Name the blood parasite species.
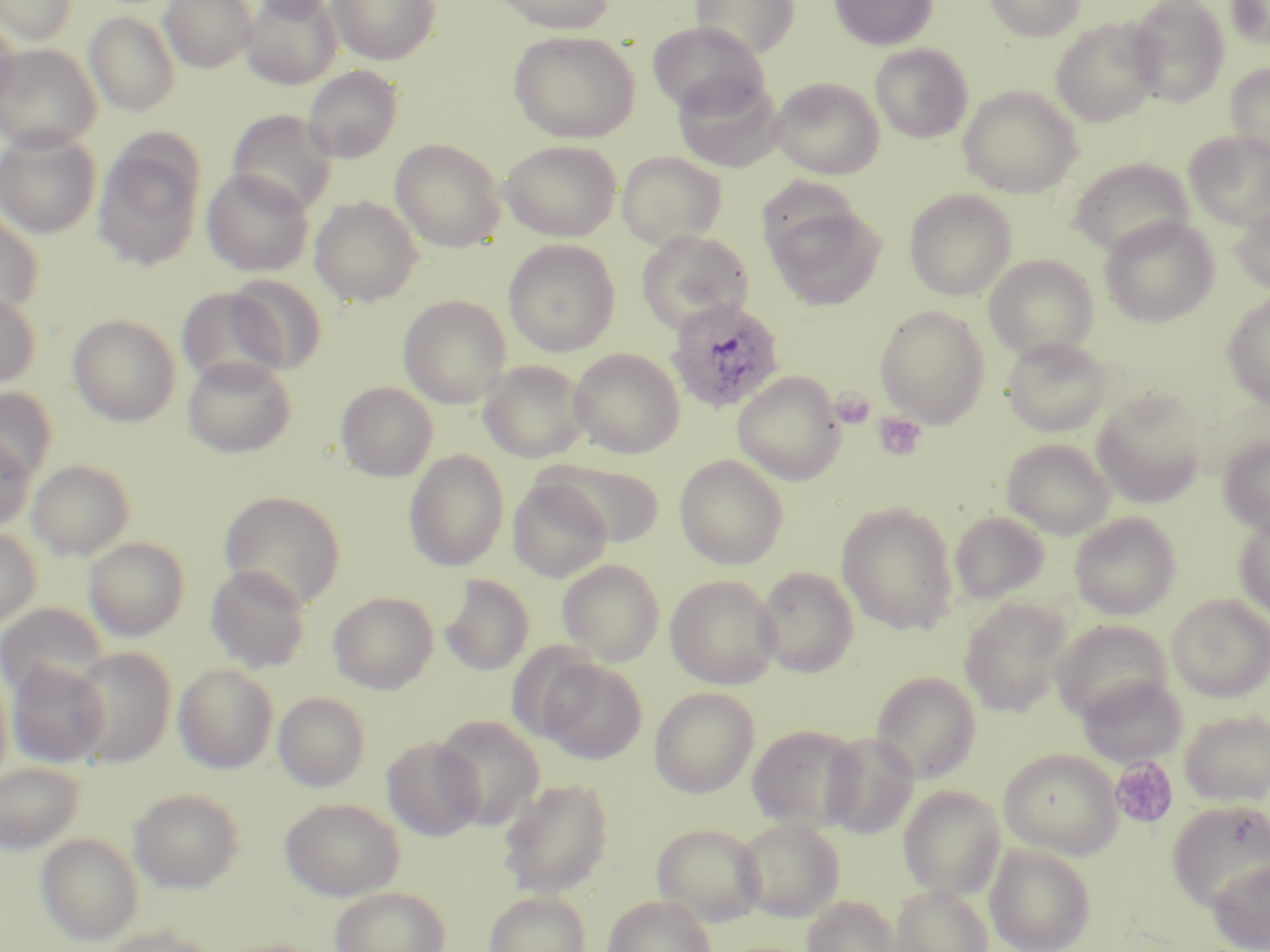

Plasmodium ovale.

Approximate bounding boxes as named x1/y1/x2/y2 corners in pixels. Platelet locations: (x1=831, y1=388, x2=876, y2=429), (x1=873, y1=413, x2=927, y2=461), (x1=1110, y1=756, x2=1179, y2=830). Uninfected red blood cell locations: (x1=1, y1=0, x2=78, y2=45), (x1=160, y1=0, x2=257, y2=73), (x1=241, y1=0, x2=342, y2=89), (x1=247, y1=0, x2=341, y2=19), (x1=328, y1=0, x2=441, y2=65), (x1=490, y1=0, x2=617, y2=34), (x1=690, y1=0, x2=800, y2=59), (x1=830, y1=0, x2=937, y2=51), (x1=984, y1=0, x2=1085, y2=41), (x1=1127, y1=0, x2=1229, y2=106), (x1=1226, y1=0, x2=1270, y2=50), (x1=84, y1=11, x2=181, y2=116), (x1=0, y1=16, x2=19, y2=115), (x1=1050, y1=17, x2=1164, y2=127), (x1=647, y1=21, x2=769, y2=118), (x1=508, y1=30, x2=641, y2=144), (x1=0, y1=43, x2=100, y2=151), (x1=871, y1=44, x2=972, y2=143), (x1=1225, y1=64, x2=1270, y2=162), (x1=302, y1=65, x2=403, y2=164), (x1=674, y1=74, x2=783, y2=173), (x1=770, y1=77, x2=885, y2=179), (x1=959, y1=86, x2=1082, y2=198), (x1=227, y1=109, x2=338, y2=217), (x1=0, y1=127, x2=102, y2=238), (x1=1184, y1=131, x2=1270, y2=229), (x1=391, y1=139, x2=506, y2=252), (x1=500, y1=139, x2=621, y2=241), (x1=93, y1=142, x2=205, y2=271), (x1=617, y1=151, x2=727, y2=249), (x1=1068, y1=157, x2=1194, y2=258), (x1=201, y1=168, x2=315, y2=277), (x1=904, y1=189, x2=1017, y2=301), (x1=310, y1=196, x2=424, y2=307), (x1=767, y1=203, x2=886, y2=311), (x1=1230, y1=204, x2=1270, y2=293), (x1=0, y1=210, x2=43, y2=318), (x1=1100, y1=216, x2=1219, y2=327), (x1=636, y1=230, x2=753, y2=334), (x1=504, y1=239, x2=621, y2=357), (x1=983, y1=254, x2=1099, y2=361), (x1=227, y1=274, x2=327, y2=373), (x1=175, y1=287, x2=290, y2=390), (x1=0, y1=289, x2=41, y2=389), (x1=1222, y1=292, x2=1270, y2=409), (x1=398, y1=295, x2=512, y2=408), (x1=874, y1=305, x2=990, y2=427), (x1=68, y1=314, x2=181, y2=427), (x1=1002, y1=336, x2=1111, y2=436), (x1=568, y1=348, x2=685, y2=458), (x1=182, y1=356, x2=296, y2=458), (x1=479, y1=360, x2=589, y2=463), (x1=732, y1=372, x2=846, y2=485), (x1=336, y1=381, x2=437, y2=481), (x1=0, y1=387, x2=57, y2=484), (x1=1091, y1=388, x2=1207, y2=507), (x1=0, y1=432, x2=35, y2=532), (x1=1219, y1=435, x2=1270, y2=537), (x1=1001, y1=438, x2=1115, y2=538), (x1=404, y1=449, x2=509, y2=572), (x1=674, y1=454, x2=789, y2=569), (x1=536, y1=458, x2=666, y2=546), (x1=28, y1=459, x2=135, y2=560), (x1=508, y1=478, x2=613, y2=582), (x1=219, y1=490, x2=346, y2=609), (x1=837, y1=502, x2=958, y2=634), (x1=950, y1=510, x2=1049, y2=605), (x1=1070, y1=513, x2=1180, y2=619), (x1=1234, y1=513, x2=1270, y2=621), (x1=0, y1=526, x2=41, y2=630), (x1=84, y1=537, x2=188, y2=642), (x1=557, y1=559, x2=665, y2=664), (x1=206, y1=564, x2=312, y2=672), (x1=558, y1=564, x2=780, y2=673), (x1=754, y1=566, x2=859, y2=677), (x1=439, y1=574, x2=534, y2=676), (x1=665, y1=574, x2=781, y2=689), (x1=328, y1=591, x2=438, y2=694), (x1=1168, y1=594, x2=1270, y2=701), (x1=958, y1=597, x2=1071, y2=717), (x1=0, y1=603, x2=107, y2=699), (x1=1051, y1=619, x2=1174, y2=723), (x1=69, y1=647, x2=175, y2=767), (x1=537, y1=656, x2=646, y2=763), (x1=6, y1=661, x2=110, y2=768), (x1=173, y1=663, x2=278, y2=773), (x1=0, y1=665, x2=13, y2=788), (x1=871, y1=672, x2=981, y2=783), (x1=1077, y1=673, x2=1188, y2=768), (x1=649, y1=687, x2=759, y2=798), (x1=273, y1=691, x2=370, y2=791), (x1=1180, y1=708, x2=1270, y2=805), (x1=434, y1=715, x2=545, y2=828), (x1=748, y1=724, x2=864, y2=831), (x1=820, y1=732, x2=919, y2=838), (x1=382, y1=736, x2=485, y2=841), (x1=998, y1=749, x2=1122, y2=857), (x1=0, y1=762, x2=85, y2=855), (x1=499, y1=778, x2=614, y2=897), (x1=898, y1=785, x2=1005, y2=898), (x1=129, y1=788, x2=245, y2=893), (x1=280, y1=797, x2=404, y2=900), (x1=1167, y1=800, x2=1270, y2=911), (x1=734, y1=818, x2=845, y2=921), (x1=653, y1=823, x2=766, y2=925), (x1=36, y1=833, x2=144, y2=946), (x1=985, y1=843, x2=1096, y2=952), (x1=1208, y1=856, x2=1270, y2=952), (x1=889, y1=884, x2=993, y2=952), (x1=330, y1=886, x2=451, y2=952), (x1=484, y1=891, x2=591, y2=952), (x1=603, y1=895, x2=717, y2=952), (x1=803, y1=896, x2=899, y2=952), (x1=100, y1=925, x2=220, y2=952). Plasmodium ovale-infected red blood cell locations: (x1=666, y1=298, x2=785, y2=414). 1000x magnification. May-Grünwald-Giemsa-stained preparation. Thin blood smear. One field of a larger specimen. Image is 1270×952 pixels. Optical microscopy.